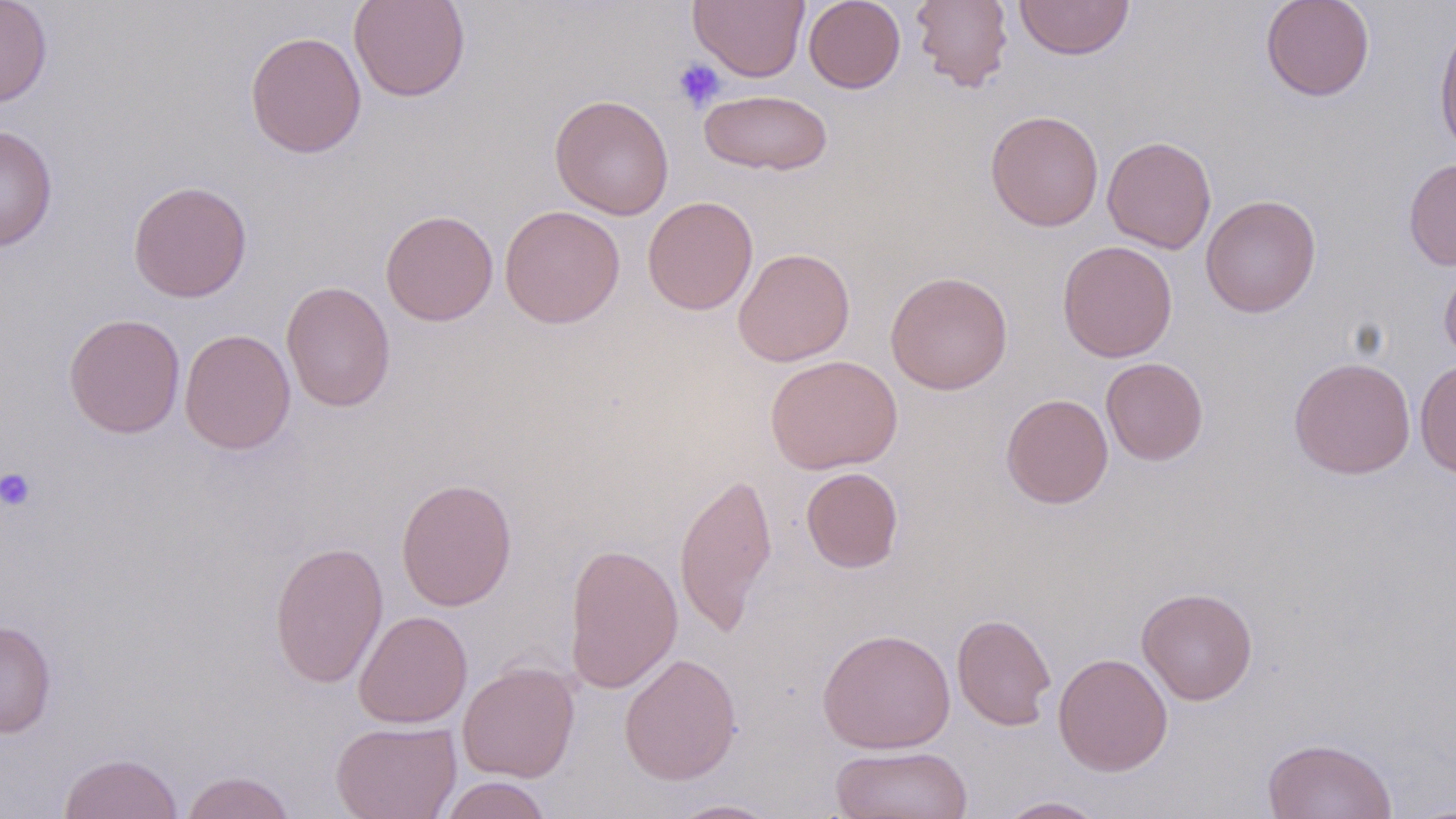 Approximate bounding boxes as (x1, y1, x2, y2) in pixels. Platelet locations: (672, 58, 726, 112), (0, 467, 37, 513). Uninfected red blood cell locations: (0, 0, 53, 108), (348, 0, 471, 102), (688, 0, 809, 82), (804, 0, 906, 93), (910, 0, 1014, 92), (1014, 0, 1135, 60), (1260, 0, 1375, 102), (1433, 19, 1456, 161), (244, 31, 367, 158), (699, 89, 833, 176), (549, 94, 674, 219), (985, 110, 1104, 232), (1, 125, 58, 251), (1102, 136, 1216, 254), (1403, 157, 1456, 270), (128, 180, 253, 303), (1200, 194, 1322, 317), (642, 196, 758, 315), (499, 204, 625, 328), (380, 209, 498, 326), (1057, 240, 1178, 362), (733, 247, 855, 367), (1439, 258, 1456, 366), (885, 271, 1013, 395), (280, 280, 396, 412), (62, 313, 185, 438), (179, 328, 296, 455), (765, 355, 902, 474), (1101, 357, 1208, 465), (1288, 357, 1416, 479), (1414, 359, 1456, 479), (1001, 393, 1113, 509), (801, 467, 904, 573), (674, 470, 778, 636), (395, 478, 518, 611), (269, 540, 389, 688), (564, 542, 684, 693), (1136, 587, 1258, 705), (353, 610, 472, 728), (952, 613, 1056, 730), (0, 620, 57, 738), (816, 628, 956, 754), (619, 652, 743, 785), (1053, 652, 1173, 776), (457, 661, 580, 782), (331, 719, 462, 819), (1261, 737, 1398, 819), (831, 745, 973, 818), (58, 752, 183, 819), (180, 770, 297, 819), (438, 776, 552, 819), (996, 796, 1109, 818), (668, 798, 785, 818). Slide-level diagnosis: no evidence of blood parasites. Thin blood smear. Single field of view. May-Grünwald-Giemsa stain. Image is 1456×819 pixels. Optical microscopy. 1000x magnification.